Point out each leukocyte.
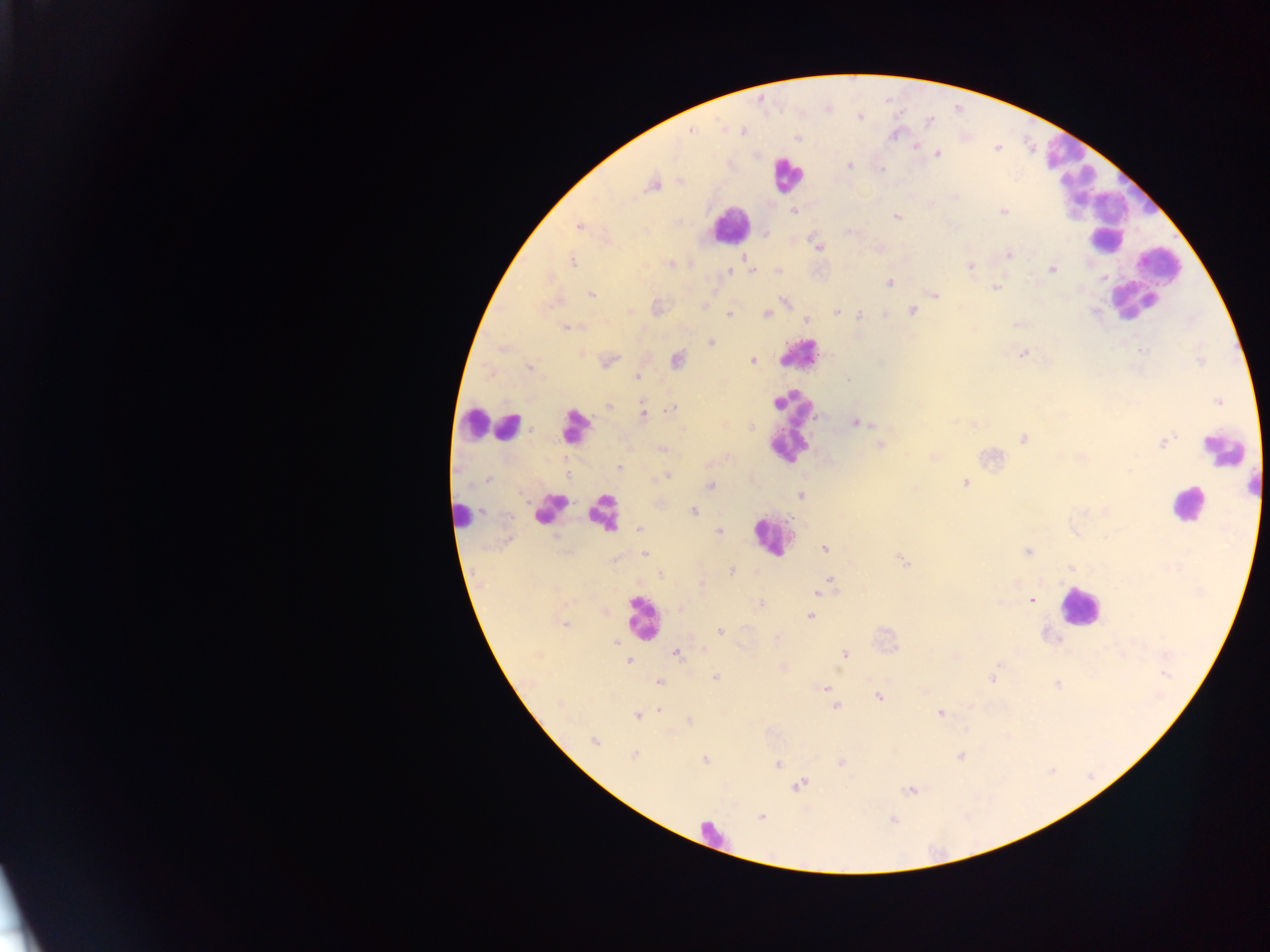
Approximate centers as [x, y] in pixels.
Leukocytes: [1059, 150], [786, 173], [1075, 188], [1122, 206], [729, 224], [1105, 241], [1156, 269], [1137, 300], [799, 352], [474, 424], [509, 425], [575, 426], [791, 428], [1225, 452], [1186, 505], [550, 508], [602, 510], [463, 514], [770, 537], [1079, 607], [641, 616], [716, 834].

preparation = thick blood film
country = Ghana
malaria parasite locations = approximate centers as [x, y] in pixels: [859, 117], [930, 120], [742, 130], [692, 131], [895, 135], [798, 138], [916, 145], [938, 153], [849, 166], [882, 169], [680, 180], [651, 185], [794, 211], [1003, 212], [897, 216], [579, 227], [849, 231], [766, 233], [818, 247], [1009, 254], [744, 258], [572, 261], [670, 263], [971, 266], [1053, 269], [751, 270], [729, 271], [778, 272], [1102, 277], [889, 283], [997, 287], [592, 294], [934, 295], [785, 301], [655, 308], [837, 311], [912, 311], [1095, 311], [766, 313], [728, 314], [860, 315], [884, 315], [807, 320], [1016, 324], [568, 327], [711, 342], [1140, 350], [1023, 353], [677, 359], [753, 360], [609, 362], [529, 367], [638, 377], [848, 380], [1218, 401], [608, 405], [672, 408], [643, 413], [856, 422], [973, 425], [1024, 439], [1165, 442], [879, 445], [662, 449], [1083, 457], [620, 468], [667, 477], [488, 480], [965, 483], [711, 485], [801, 495], [693, 511], [639, 529], [718, 532], [823, 548], [1028, 552], [645, 554], [903, 561], [1071, 568], [732, 571], [660, 574], [830, 580], [818, 592], [1031, 600], [761, 605], [810, 616], [564, 624], [719, 631], [776, 638], [615, 641], [676, 653], [845, 654], [629, 660], [1165, 674], [994, 676], [715, 677], [659, 682], [1057, 684], [825, 688], [879, 697], [558, 703], [836, 706], [660, 710], [939, 714], [637, 716], [689, 720], [594, 741], [635, 755], [961, 757], [705, 760], [778, 763], [841, 763], [799, 785], [909, 790], [761, 817], [892, 820]
field of view = single
capture = mobile-phone photograph through a microscope
image size = 1270×952 pixels